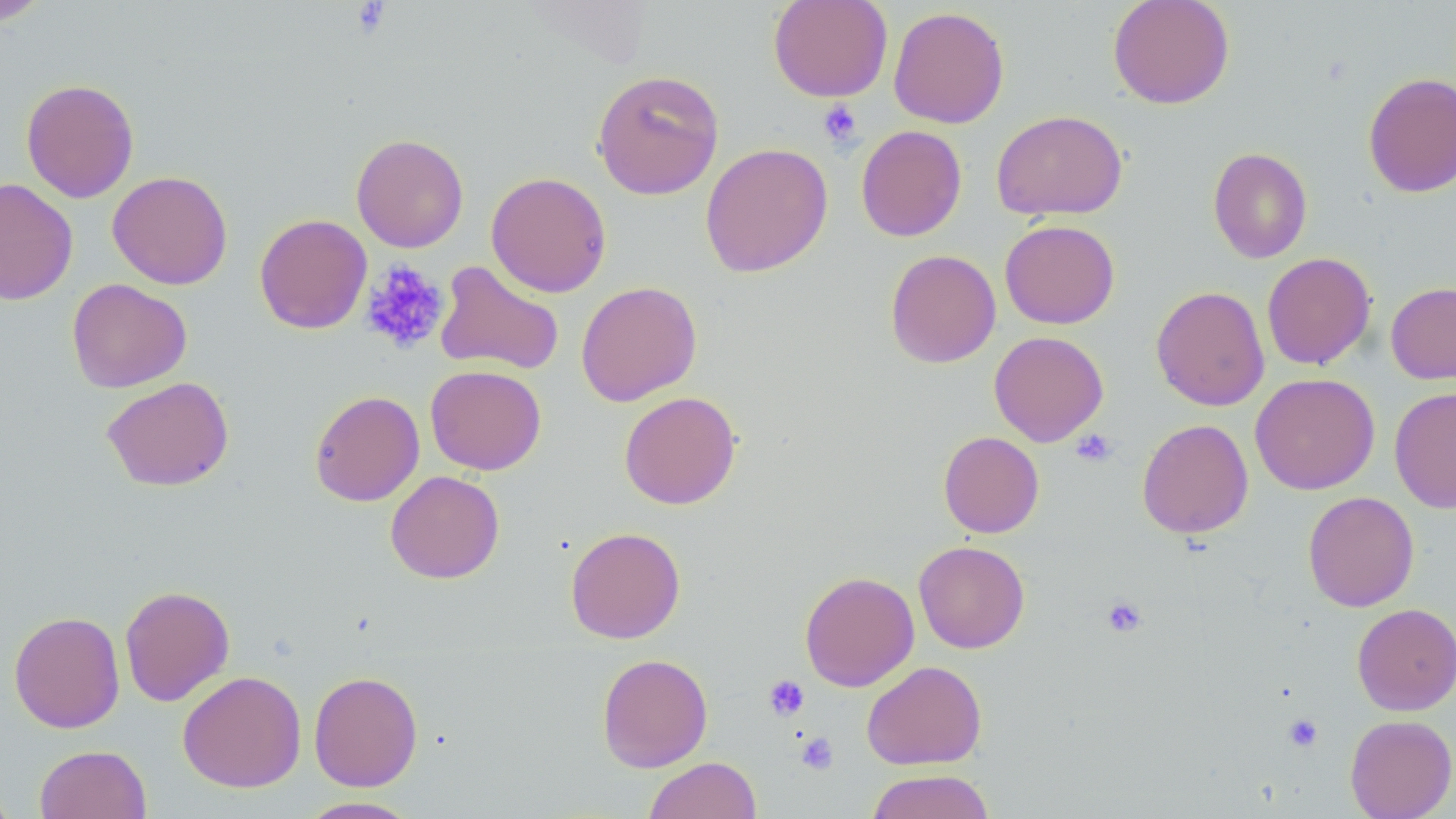
Approximate bounding boxes as named x1/y1/x2/y2 corners in pixels. Uninfected red blood cell locations: (x1=0, y1=0, x2=52, y2=26), (x1=768, y1=0, x2=893, y2=102), (x1=1107, y1=0, x2=1235, y2=109), (x1=888, y1=6, x2=1010, y2=128), (x1=592, y1=68, x2=724, y2=200), (x1=1363, y1=71, x2=1456, y2=198), (x1=20, y1=78, x2=139, y2=203), (x1=991, y1=110, x2=1128, y2=221), (x1=855, y1=125, x2=967, y2=242), (x1=351, y1=133, x2=469, y2=252), (x1=700, y1=142, x2=833, y2=278), (x1=1207, y1=147, x2=1313, y2=263), (x1=107, y1=170, x2=233, y2=289), (x1=485, y1=172, x2=612, y2=297), (x1=0, y1=178, x2=78, y2=305), (x1=254, y1=213, x2=373, y2=334), (x1=1000, y1=220, x2=1120, y2=329), (x1=885, y1=249, x2=1001, y2=368), (x1=1261, y1=252, x2=1376, y2=370), (x1=435, y1=261, x2=564, y2=376), (x1=66, y1=278, x2=192, y2=393), (x1=575, y1=281, x2=702, y2=406), (x1=1386, y1=281, x2=1456, y2=384), (x1=1151, y1=285, x2=1270, y2=411), (x1=989, y1=331, x2=1108, y2=446), (x1=425, y1=365, x2=547, y2=475), (x1=1250, y1=373, x2=1380, y2=495), (x1=101, y1=376, x2=234, y2=491), (x1=1389, y1=386, x2=1456, y2=513), (x1=309, y1=390, x2=425, y2=506), (x1=619, y1=391, x2=741, y2=509), (x1=1137, y1=419, x2=1254, y2=538), (x1=938, y1=431, x2=1044, y2=538), (x1=385, y1=470, x2=505, y2=584), (x1=1303, y1=491, x2=1420, y2=612), (x1=565, y1=526, x2=686, y2=643), (x1=914, y1=540, x2=1030, y2=653), (x1=799, y1=571, x2=919, y2=691), (x1=119, y1=585, x2=235, y2=706), (x1=1352, y1=603, x2=1456, y2=715), (x1=9, y1=611, x2=125, y2=733), (x1=596, y1=653, x2=713, y2=772), (x1=861, y1=660, x2=987, y2=770), (x1=177, y1=670, x2=306, y2=793), (x1=308, y1=670, x2=423, y2=791), (x1=1344, y1=714, x2=1456, y2=819), (x1=35, y1=744, x2=152, y2=819), (x1=644, y1=757, x2=762, y2=819), (x1=866, y1=769, x2=995, y2=819), (x1=0, y1=775, x2=17, y2=819), (x1=295, y1=796, x2=424, y2=818). Platelet locations: (x1=350, y1=2, x2=392, y2=38), (x1=818, y1=100, x2=862, y2=148), (x1=359, y1=260, x2=451, y2=355), (x1=1070, y1=429, x2=1117, y2=467), (x1=1102, y1=595, x2=1148, y2=638), (x1=763, y1=674, x2=810, y2=721), (x1=1283, y1=713, x2=1323, y2=752), (x1=795, y1=732, x2=839, y2=775). Slide-level diagnosis: negative for blood parasites. Light microscopy. 1000x magnification. Image is 1456×819 pixels. One field of a larger specimen. Thin blood smear. May-Grünwald-Giemsa stain.